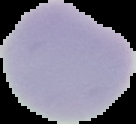
image_size: 136×124 pixels
image_type: segmented cell region with the area outside set to black
malaria_status: uninfected
preparation: thin blood film